Report the malaria status of this cell.
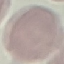
It is uninfected.

Acquired by smartphone through the microscope eyepiece. Automatically extracted cell patch, resized to 64 × 64 pixels. Thin blood smear. Giemsa-stained preparation.